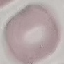

Result: no malaria parasites seen. Giemsa stain. Thin blood film. Acquired by smartphone through the microscope eyepiece. Automatically extracted cell patch, resized to 64 × 64 pixels.